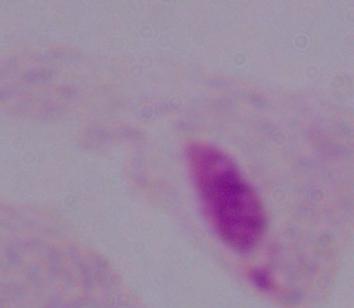
modality = micrograph
magnification = 1000x
identification = trichomonad